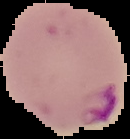
Summary:
  - Image type: cell region segmented out of the field of view; surrounding area masked to black
  - Preparation: thin blood film
  - Image size: 130×139 pixels
  - Malaria status: parasitized